Give the position of every Plasmodium parasite.
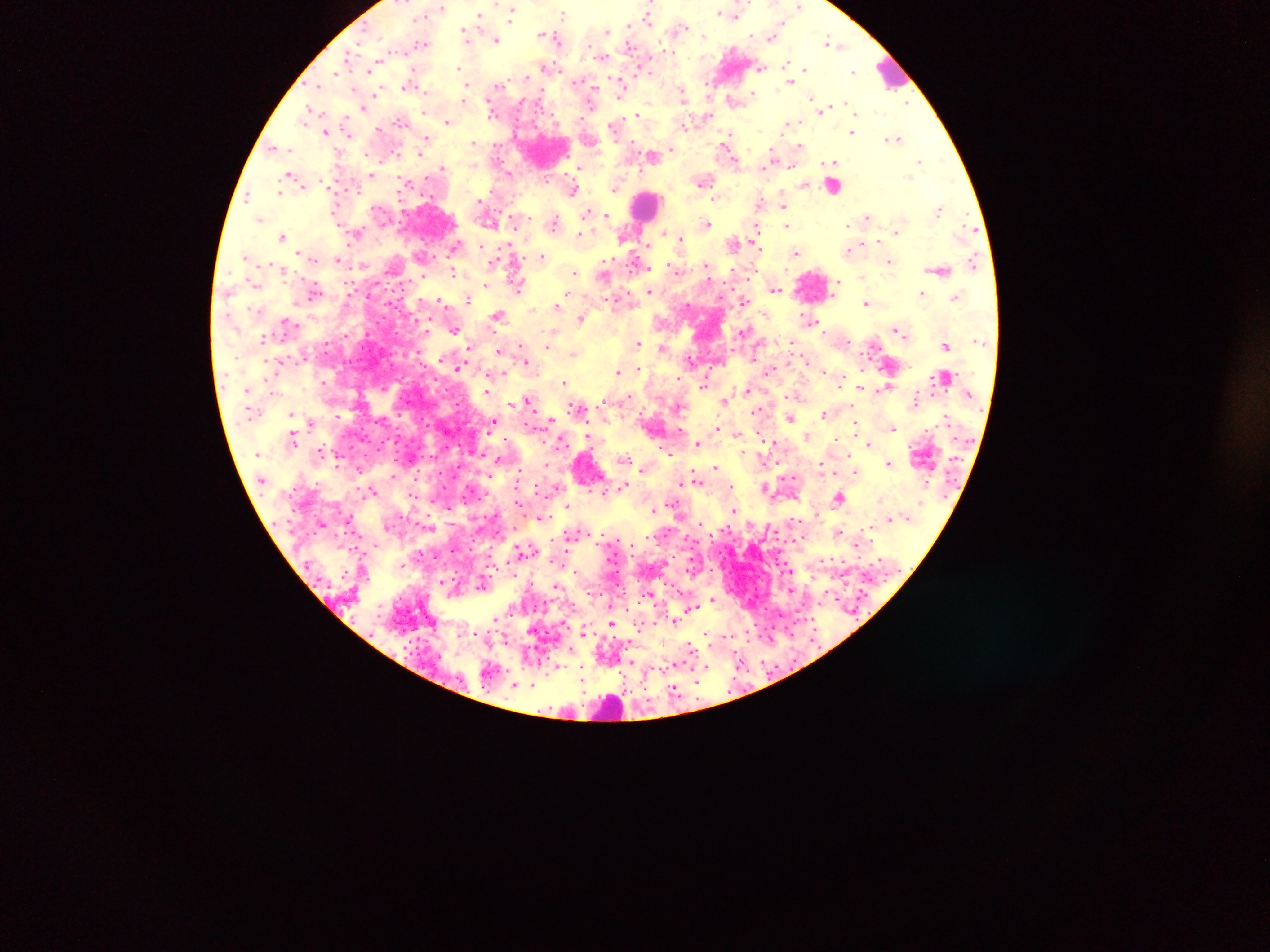

Approximate centers as (x, y) in pixels.
Plasmodium parasites: (799, 6), (441, 8), (511, 11), (731, 13), (564, 15), (649, 15), (480, 16), (630, 26), (682, 26), (606, 31), (546, 33), (773, 34), (467, 35), (554, 37), (495, 39), (423, 43), (833, 43), (665, 51), (604, 56), (547, 66), (787, 66), (760, 67), (460, 68), (805, 69), (854, 72), (528, 76), (790, 81), (621, 83), (318, 85), (410, 85), (498, 86), (465, 87), (683, 94), (376, 95), (754, 95), (465, 98), (812, 98), (733, 99), (846, 103), (362, 107), (822, 108), (493, 113), (639, 114), (707, 114), (310, 115), (399, 120), (447, 121), (789, 122), (615, 124), (684, 125), (323, 127), (379, 128), (852, 131), (326, 132), (425, 138), (894, 138), (473, 141), (273, 146), (800, 146), (728, 149), (420, 153), (653, 155), (773, 161), (920, 162), (834, 163), (443, 167), (580, 169), (509, 173), (371, 174), (293, 177), (703, 180), (297, 181), (804, 184), (617, 186), (574, 189), (280, 192), (248, 195), (480, 201), (760, 201), (784, 202), (939, 209), (587, 212), (605, 215), (868, 217), (260, 218), (554, 223), (707, 224), (786, 225), (756, 227), (356, 232), (664, 233), (581, 235), (282, 236), (623, 237), (680, 238), (878, 239), (734, 243), (849, 250), (797, 252), (247, 256), (542, 256), (337, 259), (495, 260), (890, 261), (974, 263), (706, 265), (281, 267), (675, 269), (940, 269), (576, 271), (454, 272), (486, 285), (518, 286), (775, 289), (316, 291), (649, 291), (569, 292), (922, 293), (958, 296), (468, 298), (443, 300), (743, 300), (866, 303), (557, 304), (498, 316), (580, 317), (808, 318), (288, 322), (455, 329), (899, 331), (264, 337), (792, 341), (637, 344), (548, 345), (946, 345), (470, 347), (662, 348), (499, 351), (574, 352), (691, 360), (527, 361), (458, 365), (637, 368), (824, 369), (771, 370), (619, 372), (492, 376), (564, 382), (323, 383), (705, 383), (861, 386), (884, 388), (746, 390), (488, 391), (915, 399), (529, 400), (725, 400), (578, 408), (757, 410), (825, 413), (291, 415), (337, 416), (790, 417), (552, 420), (494, 421), (311, 423), (855, 425), (717, 427), (893, 427), (738, 432), (589, 436), (807, 436), (293, 437), (561, 440), (771, 441), (698, 442), (869, 442), (321, 452), (742, 452), (624, 458), (890, 463), (715, 467), (643, 468), (822, 468), (360, 469), (520, 470), (856, 472), (696, 477), (681, 481), (626, 485), (765, 487), (557, 488), (372, 491), (840, 497), (568, 504), (655, 510), (735, 510), (322, 523), (839, 532), (572, 534), (524, 550), (402, 564), (441, 581), (483, 585), (557, 585), (649, 593), (712, 599), (690, 608), (496, 617), (675, 621), (611, 623), (583, 631), (691, 646), (631, 662), (557, 666), (707, 667), (584, 672), (698, 679), (533, 685), (515, 686), (674, 689).

Summary:
  - Leukocyte locations: (892, 72), (833, 186), (645, 207), (813, 285), (589, 468), (609, 707)
  - Preparation: thick blood smear
  - Image size: 1270×952 pixels
  - Country: Ghana
  - Capture: mobile-phone photograph through a microscope
  - Field of view: single